Name the blood parasite species.
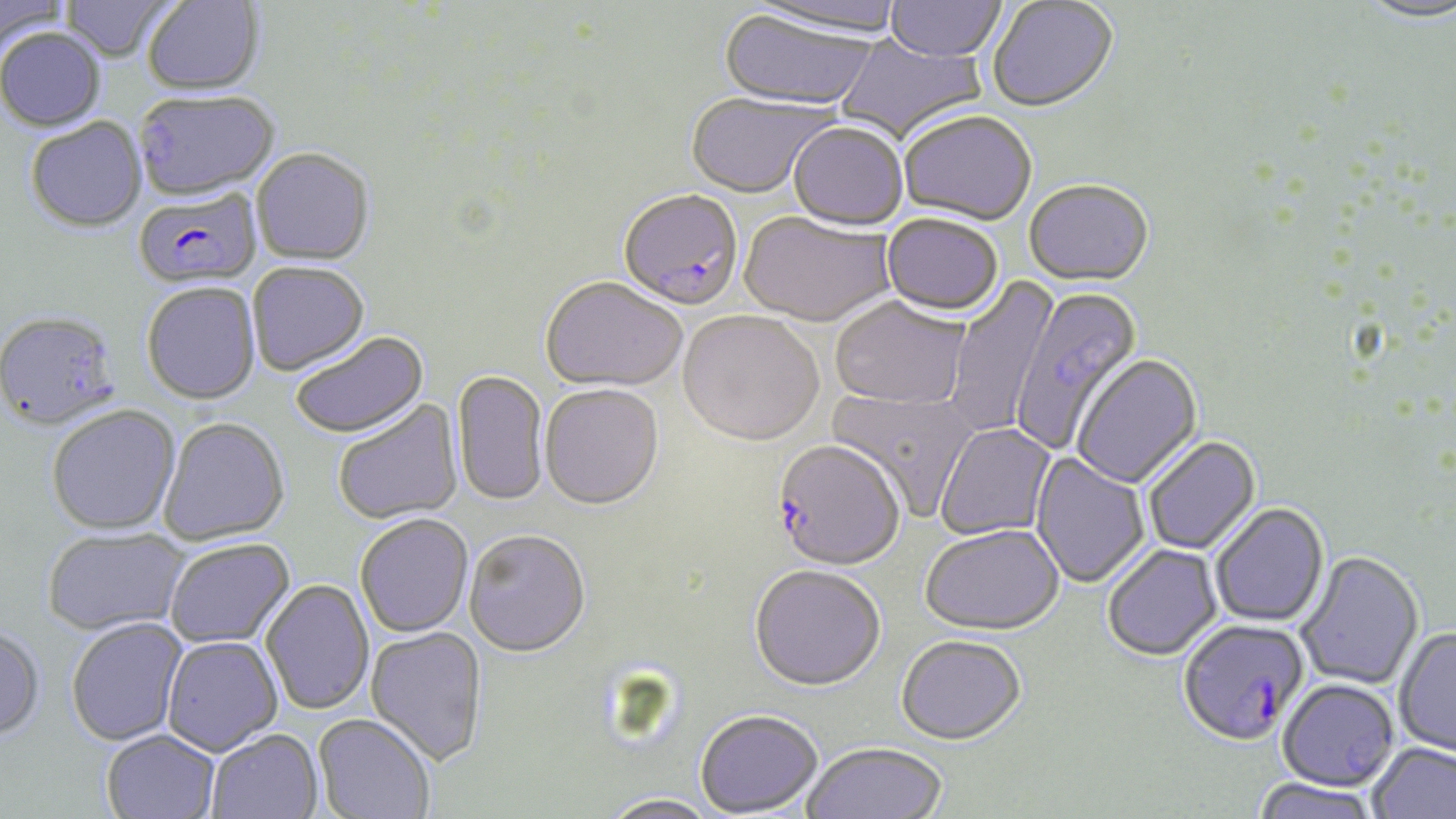

Plasmodium falciparum.

modality = optical microscopy
uninfected red blood cell locations = approximate bounding boxes as [x1, y1, x2, y2] in pixels: [0, 0, 70, 55], [60, 0, 177, 64], [142, 0, 265, 98], [744, 0, 907, 43], [885, 0, 1007, 64], [987, 1, 1119, 115], [1355, 1, 1456, 28], [718, 12, 876, 113], [0, 30, 106, 134], [833, 34, 987, 145], [133, 94, 281, 205], [685, 94, 836, 201], [898, 113, 1037, 228], [25, 119, 148, 235], [787, 124, 908, 233], [250, 151, 374, 268], [1023, 182, 1154, 291], [738, 213, 897, 331], [881, 216, 1003, 319], [248, 264, 370, 378], [946, 274, 1059, 436], [540, 279, 687, 395], [141, 284, 261, 407], [1011, 286, 1144, 455], [830, 299, 970, 411], [677, 313, 824, 450], [0, 314, 122, 435], [291, 334, 429, 441], [1071, 355, 1203, 490], [451, 371, 549, 508], [539, 386, 664, 513], [828, 386, 982, 519], [333, 399, 464, 527], [47, 407, 182, 538], [159, 420, 290, 546], [936, 423, 1058, 541], [1143, 437, 1262, 557], [1030, 451, 1150, 590], [1210, 504, 1330, 629], [355, 516, 474, 639], [920, 527, 1064, 638], [42, 529, 191, 638], [464, 532, 591, 660], [165, 540, 296, 650], [1103, 545, 1223, 663], [1295, 552, 1424, 690], [748, 568, 886, 694], [261, 580, 374, 717], [67, 618, 188, 747], [0, 626, 47, 742], [365, 627, 488, 767], [1394, 627, 1456, 760], [161, 637, 283, 758], [896, 637, 1026, 746], [1277, 679, 1399, 792], [695, 710, 824, 817], [312, 715, 435, 818], [101, 730, 221, 819], [207, 730, 324, 819], [803, 742, 946, 819], [1367, 742, 1456, 819], [1250, 779, 1383, 819], [598, 795, 722, 819]
preparation = thin blood film
field of view = one of a larger specimen
stain = May-Grünwald-Giemsa
Plasmodium falciparum-infected red blood cell locations = approximate bounding boxes as [x1, y1, x2, y2] in pixels: [133, 189, 262, 290], [618, 191, 744, 313], [771, 443, 905, 573], [1177, 619, 1310, 747]
magnification = 1000x
image size = 1456×819 pixels